Describe the morphology of the red blood cells.
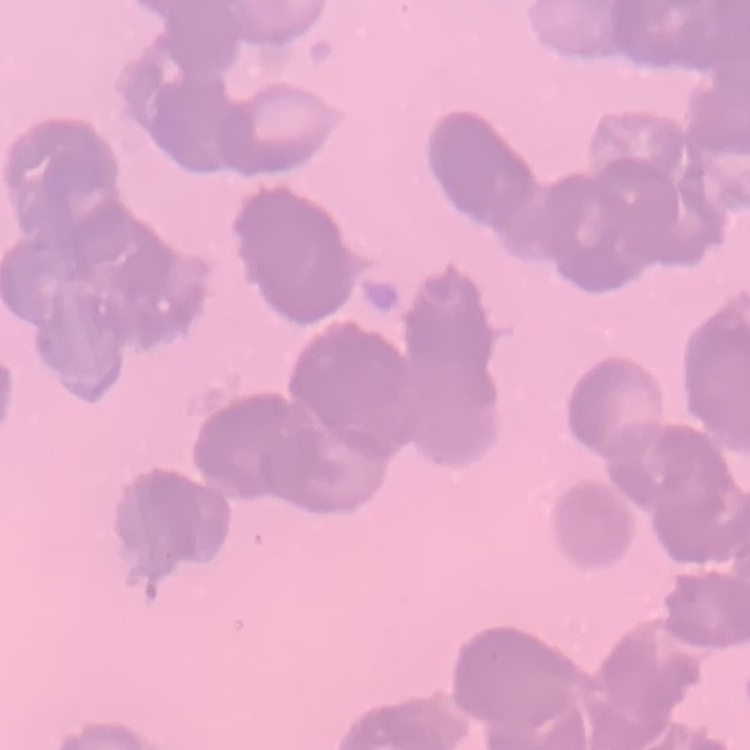

They show rouleaux formation.

Summary:
  - Image type: one tile cut from a larger photomicrograph
  - Stain: Field's or Giemsa
  - Preparation: thin blood film